Locate every blood parasite and identify its species.
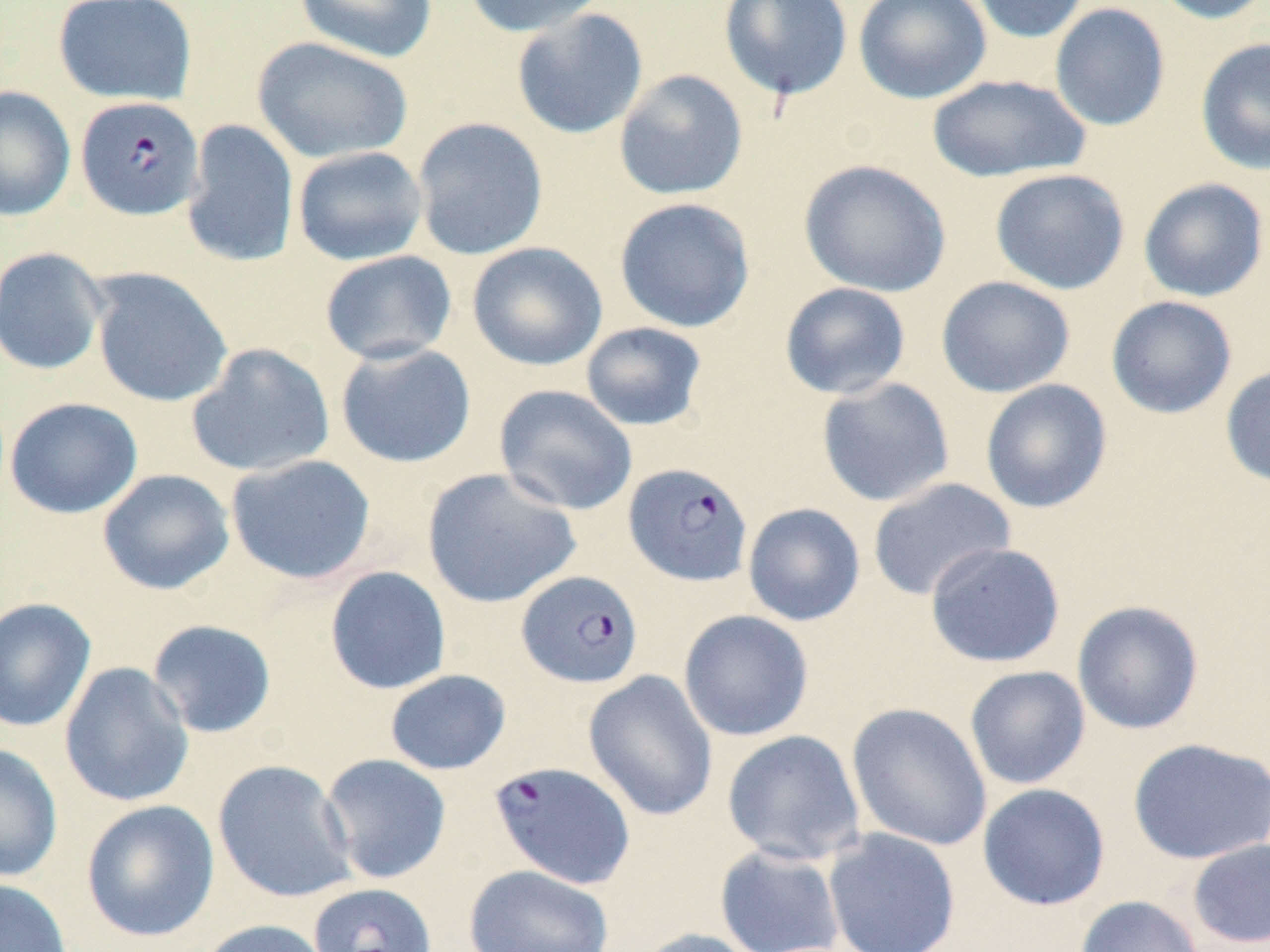

Approximate bounding boxes as named x1/y1/x2/y2 corners in pixels.
Plasmodium falciparum-infected red blood cells: (x1=75, y1=96, x2=204, y2=221), (x1=623, y1=461, x2=754, y2=587), (x1=516, y1=570, x2=643, y2=689), (x1=488, y1=761, x2=636, y2=889), (x1=308, y1=883, x2=437, y2=952).
No Plasmodium ovale, Plasmodium malariae, Plasmodium vivax, Babesia divergens, or Trypanosoma brucei observed.

Uninfected red blood cell locations: (x1=52, y1=0, x2=197, y2=106), (x1=294, y1=0, x2=438, y2=63), (x1=463, y1=0, x2=610, y2=37), (x1=718, y1=0, x2=853, y2=102), (x1=853, y1=0, x2=993, y2=104), (x1=967, y1=0, x2=1090, y2=43), (x1=1148, y1=0, x2=1270, y2=24), (x1=1049, y1=2, x2=1170, y2=131), (x1=511, y1=8, x2=648, y2=139), (x1=251, y1=37, x2=413, y2=164), (x1=1195, y1=37, x2=1270, y2=175), (x1=613, y1=69, x2=749, y2=201), (x1=927, y1=73, x2=1090, y2=183), (x1=0, y1=86, x2=76, y2=221), (x1=411, y1=116, x2=549, y2=261), (x1=182, y1=119, x2=300, y2=269), (x1=292, y1=146, x2=428, y2=266), (x1=798, y1=159, x2=952, y2=297), (x1=989, y1=168, x2=1131, y2=296), (x1=1138, y1=177, x2=1269, y2=303), (x1=613, y1=197, x2=756, y2=333), (x1=466, y1=241, x2=607, y2=372), (x1=0, y1=246, x2=109, y2=376), (x1=319, y1=250, x2=457, y2=365), (x1=90, y1=269, x2=233, y2=408), (x1=936, y1=276, x2=1076, y2=398), (x1=779, y1=282, x2=912, y2=400), (x1=1106, y1=295, x2=1238, y2=419), (x1=580, y1=321, x2=708, y2=432), (x1=335, y1=342, x2=477, y2=469), (x1=186, y1=343, x2=335, y2=478), (x1=1220, y1=365, x2=1270, y2=489), (x1=816, y1=377, x2=955, y2=507), (x1=980, y1=379, x2=1113, y2=514), (x1=493, y1=384, x2=638, y2=515), (x1=4, y1=396, x2=143, y2=519), (x1=226, y1=454, x2=377, y2=585), (x1=421, y1=468, x2=582, y2=609), (x1=97, y1=469, x2=234, y2=595), (x1=866, y1=477, x2=1016, y2=602), (x1=742, y1=503, x2=866, y2=626), (x1=925, y1=542, x2=1065, y2=668), (x1=324, y1=566, x2=451, y2=695), (x1=0, y1=597, x2=96, y2=733), (x1=1072, y1=600, x2=1205, y2=735), (x1=678, y1=609, x2=814, y2=742), (x1=146, y1=619, x2=278, y2=739), (x1=59, y1=662, x2=194, y2=808), (x1=964, y1=665, x2=1091, y2=790), (x1=384, y1=669, x2=511, y2=775), (x1=583, y1=669, x2=719, y2=822), (x1=846, y1=702, x2=992, y2=851), (x1=722, y1=730, x2=866, y2=866), (x1=1127, y1=737, x2=1270, y2=865), (x1=0, y1=743, x2=63, y2=883), (x1=319, y1=753, x2=452, y2=884), (x1=212, y1=759, x2=357, y2=903), (x1=977, y1=783, x2=1111, y2=911), (x1=80, y1=799, x2=220, y2=942), (x1=823, y1=828, x2=961, y2=952), (x1=1186, y1=838, x2=1270, y2=949), (x1=714, y1=843, x2=846, y2=952), (x1=463, y1=864, x2=614, y2=952), (x1=0, y1=878, x2=73, y2=952), (x1=1075, y1=895, x2=1204, y2=952), (x1=194, y1=918, x2=334, y2=952), (x1=633, y1=927, x2=766, y2=952). Slide-level diagnosis: Plasmodium falciparum. May-Grünwald-Giemsa-stained preparation. Thin blood smear. Single field of view. Image is 1270×952 pixels. Light microscopy. Captured at 1000x magnification.